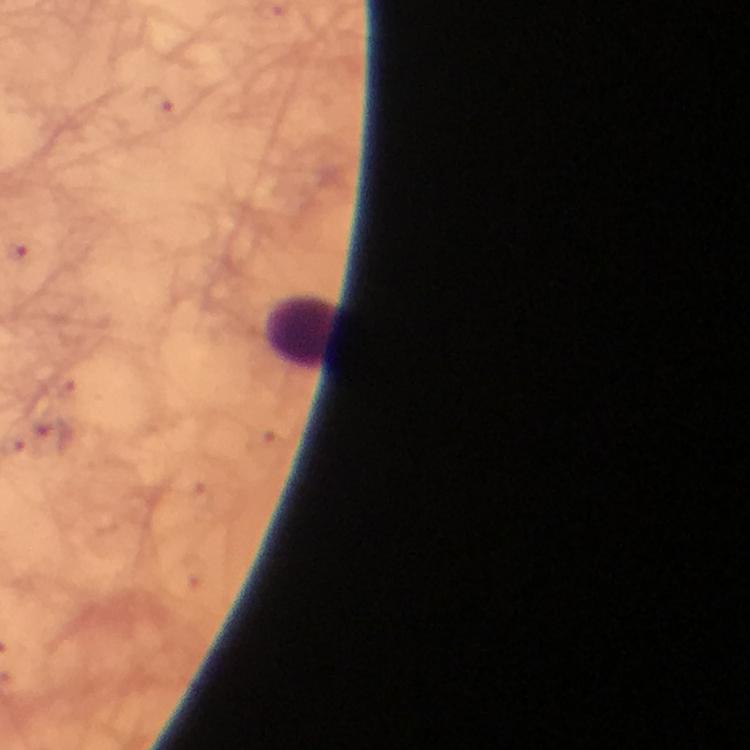
Approximate centers as {x, y} in pixels.
Summary:
  - Leukocyte locations: {302, 331}
  - Immersion oil: applied
  - Preparation: thick smear
  - Context: from a malaria diagnostic workup
  - Capture: smartphone photograph through a microscope
  - Image size: 750×750 pixels
  - Cropped from: one field of view
  - Stain: Giemsa
  - Magnification: 100x
  - Plasmodium parasites: none seen